Name the parasite shown.
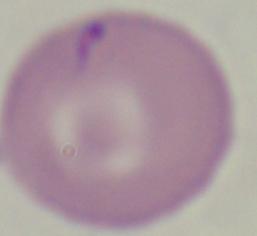
This is Babesia.

Summary:
  - Magnification: 1000x
  - Modality: micrograph